Name the parasite shown.
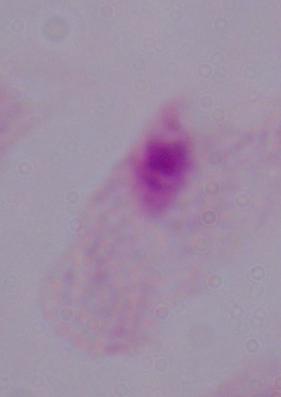

This is a trichomonad.

Captured at 1000x magnification. Micrograph.